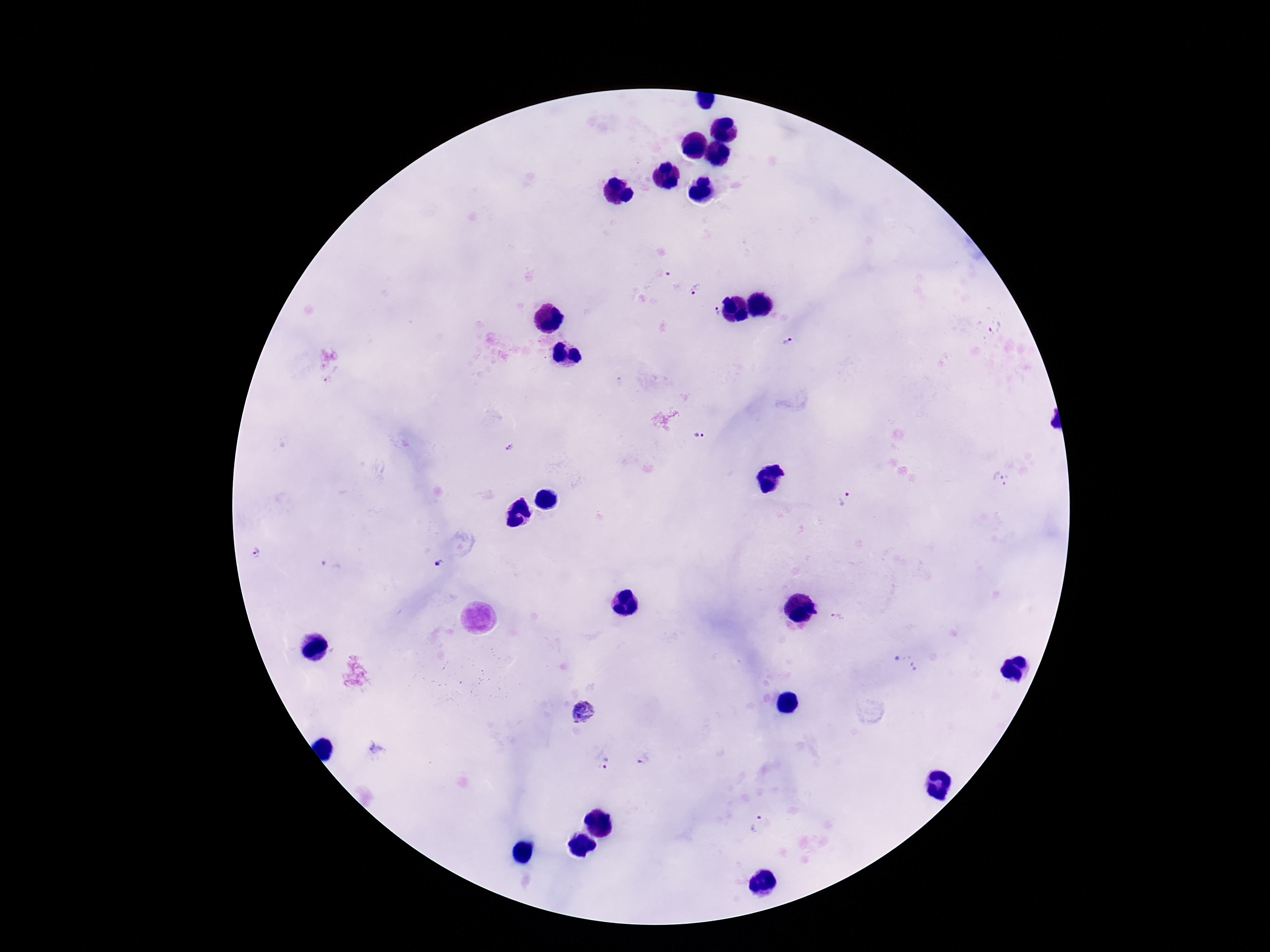
{
  "preparation": "thick peripheral-blood smear",
  "capture": "smartphone camera through the microscope eyepiece",
  "image_size": "1270×952 pixels",
  "patient_malaria_status": "infected",
  "stain": "Giemsa",
  "plasmodium_parasite_locations": "approximate centers as (x, y) in pixels: (664, 274), (697, 289), (715, 312), (995, 328), (788, 341), (701, 437), (510, 448), (1002, 479), (845, 502), (255, 553), (439, 562), (331, 564), (838, 620), (906, 664), (584, 712), (377, 748), (644, 761), (602, 764), (760, 824)",
  "magnification": "100x",
  "field_of_view": "one from this slide"
}